Report the malaria status of this cell.
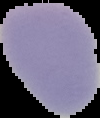

It is uninfected.

image_size: 100×118 pixels
preparation: thin blood smear
image_type: segmented cell region on a black background